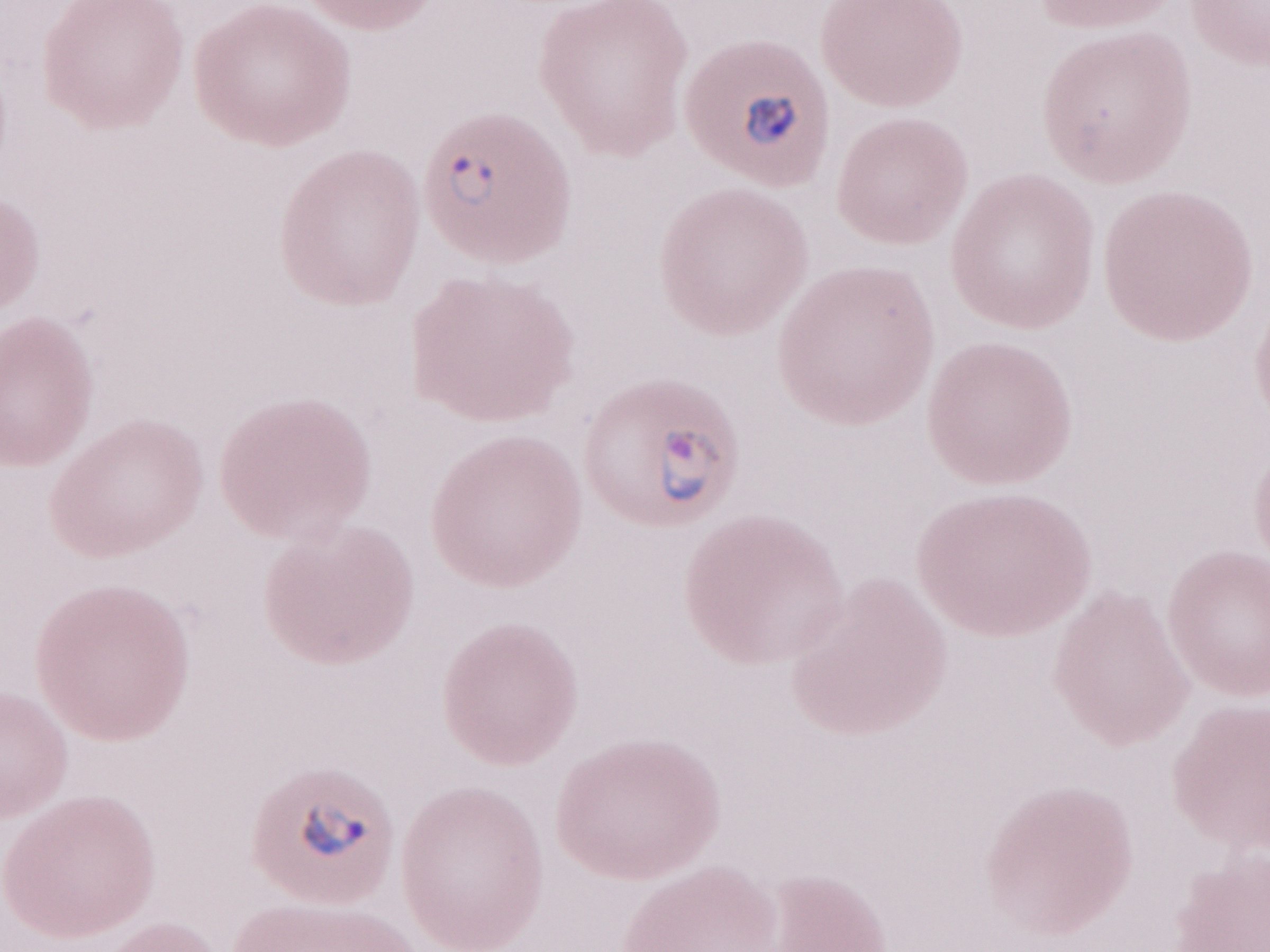
Olympus BX43 microscope, Olympus DP73 camera. Thin blood film. Magnification: 1,000x. Image is 1270×952 pixels. May-Grünwald-Giemsa-stained preparation. Patient-level malaria diagnosis: positive. One field of this slide.